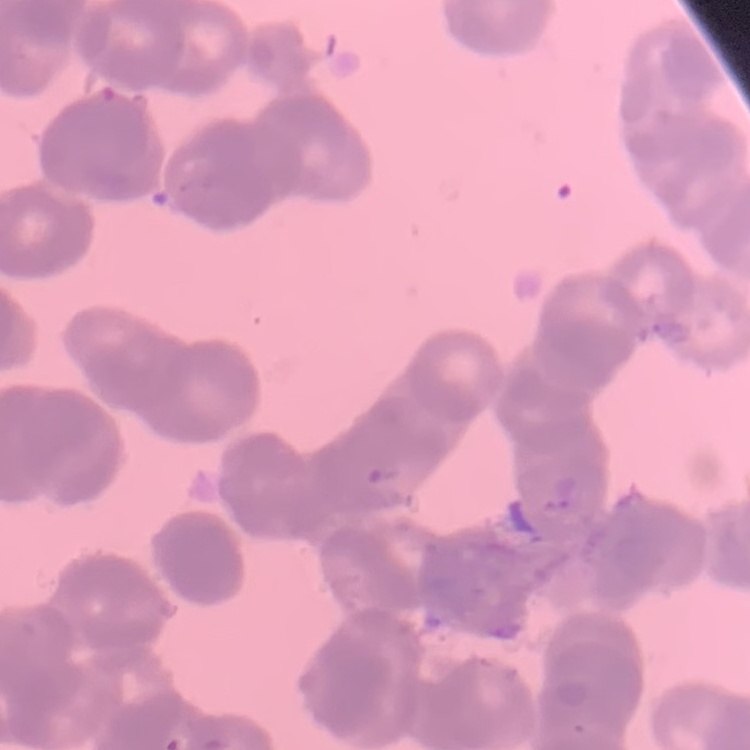

red blood cell morphology = rouleaux formation
stain = Field's or Giemsa
preparation = thin peripheral smear
image type = square crop of a larger photomicrograph